Classify this cell by malaria status.
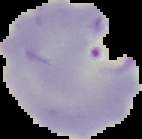

It is parasitized.

Summary:
  - Image type: segmented cell region with the area outside set to black
  - Preparation: thin blood film
  - Image size: 142×139 pixels